Outline each blood parasite and name the species.
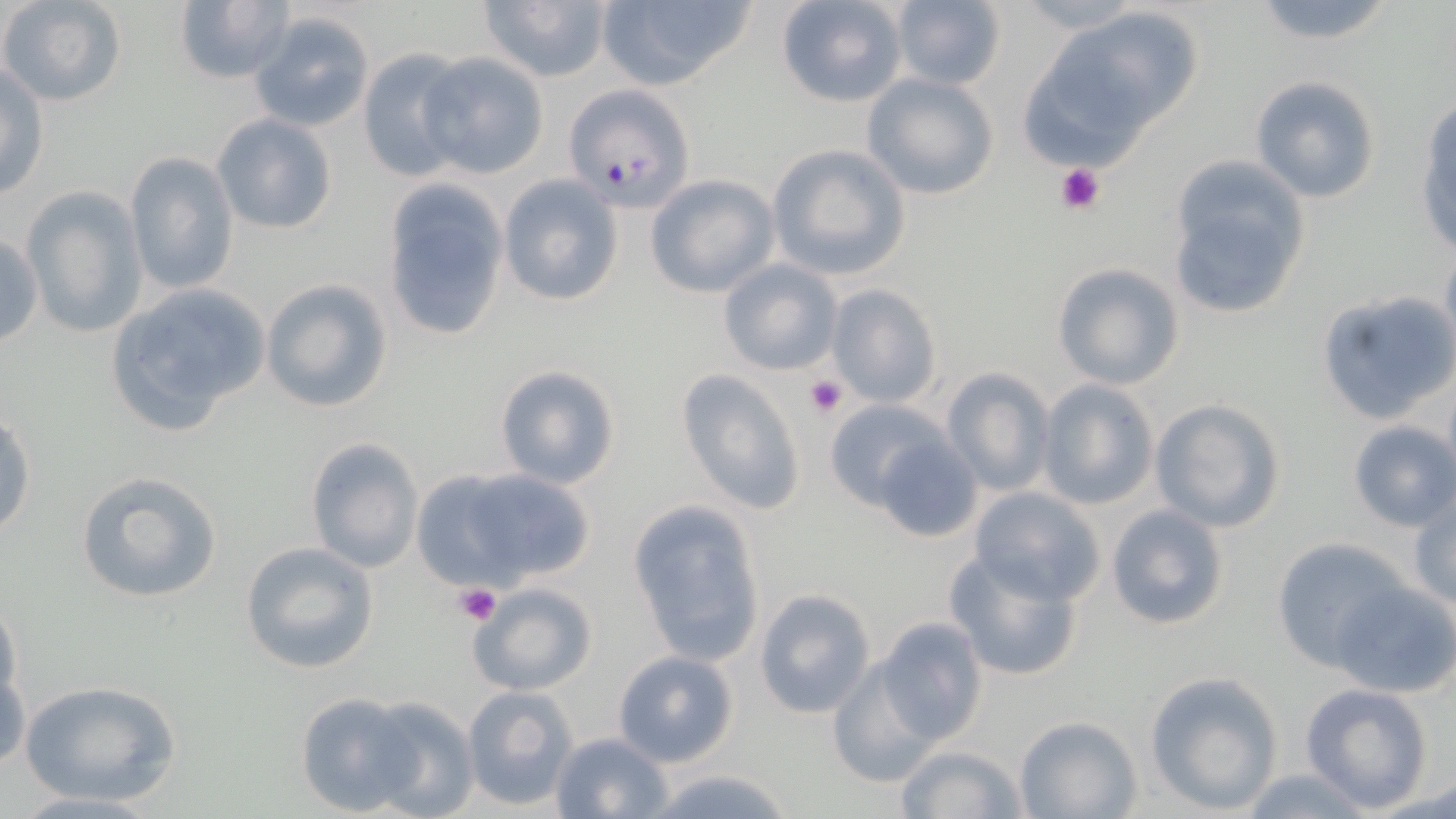

Approximate bounding boxes as [x1, y1, x2, y2] in pixels.
Plasmodium falciparum-infected red blood cells: [564, 84, 695, 212].
No Plasmodium ovale, Plasmodium malariae, Plasmodium vivax, Babesia divergens, or Trypanosoma brucei observed.

Platelet locations: [1055, 161, 1106, 212], [804, 374, 846, 419], [455, 584, 499, 626]. Uninfected red blood cell locations: [0, 0, 128, 107], [476, 0, 613, 85], [595, 0, 756, 90], [775, 0, 910, 108], [171, 1, 293, 85], [888, 1, 1010, 91], [1246, 1, 1401, 49], [1018, 10, 1199, 161], [249, 11, 376, 132], [356, 49, 473, 181], [420, 52, 550, 179], [1, 61, 50, 198], [860, 73, 998, 201], [1249, 75, 1382, 204], [1417, 101, 1456, 258], [212, 113, 337, 235], [767, 143, 913, 281], [122, 150, 240, 296], [1165, 156, 1313, 322], [645, 173, 779, 297], [499, 174, 624, 307], [380, 179, 512, 340], [20, 186, 148, 340], [0, 233, 43, 348], [1441, 243, 1456, 355], [719, 259, 842, 375], [1050, 262, 1184, 390], [260, 278, 393, 414], [825, 283, 941, 409], [102, 284, 270, 441], [1315, 290, 1456, 425], [494, 364, 620, 490], [941, 367, 1054, 495], [677, 369, 806, 514], [1036, 379, 1160, 510], [1150, 398, 1286, 532], [825, 399, 951, 511], [1, 411, 37, 539], [1347, 420, 1456, 532], [873, 435, 985, 543], [304, 436, 424, 573], [428, 464, 596, 588], [75, 469, 224, 604], [968, 486, 1107, 603], [1408, 491, 1456, 610], [627, 499, 766, 666], [1104, 503, 1230, 632], [1269, 538, 1404, 664], [240, 541, 378, 673], [944, 550, 1085, 682], [466, 579, 599, 696], [1331, 580, 1455, 698], [753, 588, 876, 719], [0, 596, 21, 710], [874, 617, 988, 744], [612, 650, 739, 767], [826, 660, 940, 789], [1, 663, 30, 774], [1144, 671, 1284, 815], [19, 678, 183, 808], [1300, 683, 1434, 812], [460, 685, 577, 810], [294, 691, 418, 815], [355, 695, 480, 819], [1014, 715, 1142, 819], [551, 732, 672, 818], [895, 744, 1028, 819], [645, 766, 798, 819], [1237, 767, 1372, 818]. Slide-level diagnosis: Plasmodium falciparum. One field of a larger specimen. Thin blood film. May-Grünwald-Giemsa-stained preparation. Light microscopy. Image is 1456×819 pixels. Captured at 1000x magnification.